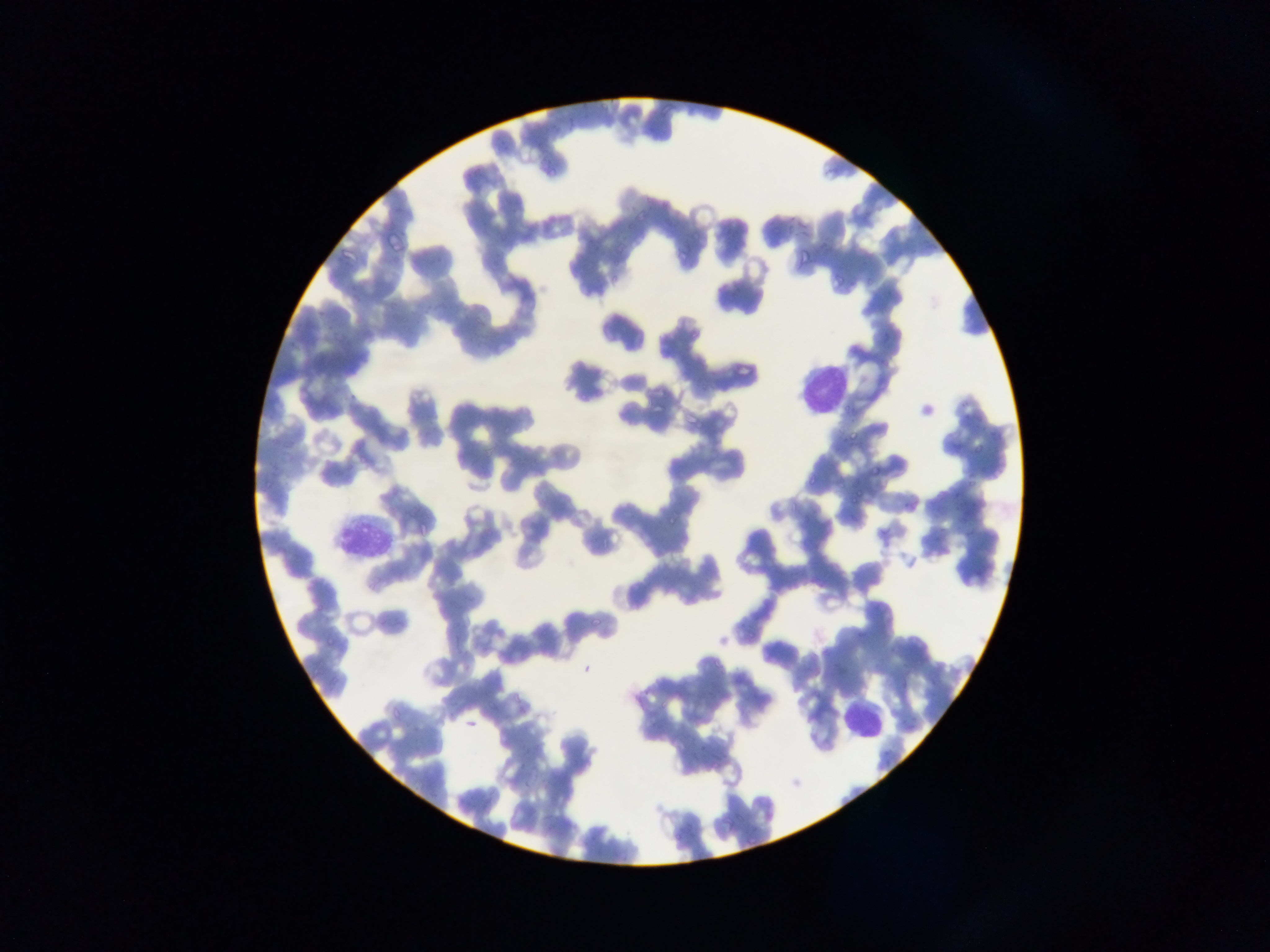
Approximate bounding boxes as (left, top, right, bottom) in pixels. Leukocyte locations: (792, 352, 850, 425), (327, 504, 395, 563), (812, 689, 886, 757). Malaria parasite locations: (832, 274, 845, 285), (687, 417, 703, 432), (847, 427, 861, 441), (967, 438, 985, 455), (868, 460, 884, 474), (803, 476, 817, 489), (850, 486, 869, 503), (662, 514, 676, 530). Sample from Ghana. Photographed through a microscope with a mobile-phone camera. Single field of view. Image is 1270×952 pixels. Thin blood film.